Assess this cell for malaria.
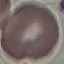
It is uninfected.

Summary:
  - Capture: smartphone camera at the microscope eyepiece
  - Stain: Giemsa
  - Image type: cell patch, automatically extracted from a larger field of view and resized to 64 × 64 pixels
  - Preparation: thin blood smear